Report the malaria status of this cell.
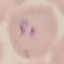
It is parasitized.

Summary:
  - Stain: Giemsa
  - Preparation: thin smear
  - Image type: cell patch, automatically extracted from a larger field of view and resized to 64 × 64 pixels
  - Capture: smartphone camera at the microscope eyepiece